Locate every Plasmodium vivax-infected red blood cell.
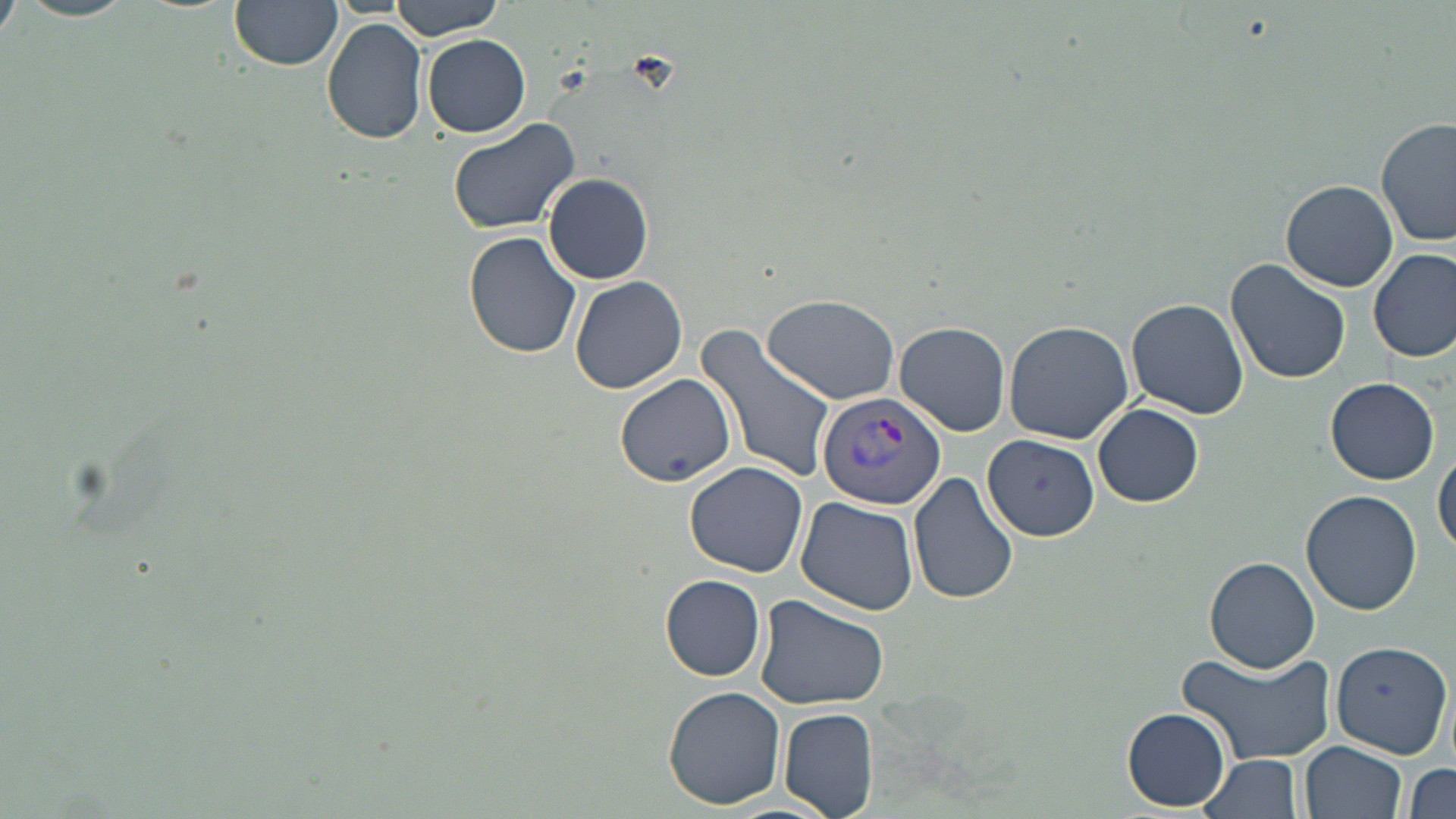

Approximate bounding boxes as named x1/y1/x2/y2 corners in pixels.
Plasmodium vivax-infected red blood cells: (x1=817, y1=392, x2=947, y2=510).

Uninfected red blood cell locations: (x1=385, y1=0, x2=509, y2=39), (x1=0, y1=1, x2=22, y2=43), (x1=229, y1=1, x2=342, y2=70), (x1=322, y1=18, x2=428, y2=144), (x1=422, y1=34, x2=531, y2=138), (x1=446, y1=117, x2=580, y2=234), (x1=1376, y1=117, x2=1456, y2=248), (x1=543, y1=174, x2=654, y2=284), (x1=1282, y1=180, x2=1398, y2=292), (x1=463, y1=231, x2=583, y2=358), (x1=1369, y1=246, x2=1456, y2=364), (x1=1225, y1=259, x2=1351, y2=385), (x1=569, y1=274, x2=688, y2=394), (x1=761, y1=292, x2=900, y2=404), (x1=1126, y1=296, x2=1249, y2=420), (x1=1003, y1=318, x2=1133, y2=444), (x1=696, y1=322, x2=836, y2=484), (x1=896, y1=322, x2=1011, y2=436), (x1=615, y1=372, x2=736, y2=487), (x1=1326, y1=377, x2=1440, y2=486), (x1=1094, y1=402, x2=1204, y2=507), (x1=984, y1=434, x2=1100, y2=542), (x1=1433, y1=449, x2=1455, y2=557), (x1=684, y1=461, x2=807, y2=577), (x1=909, y1=470, x2=1021, y2=607), (x1=1301, y1=490, x2=1422, y2=615), (x1=795, y1=497, x2=918, y2=614), (x1=1206, y1=557, x2=1320, y2=672), (x1=661, y1=575, x2=767, y2=681), (x1=754, y1=594, x2=891, y2=709), (x1=1330, y1=640, x2=1452, y2=757), (x1=1173, y1=646, x2=1336, y2=764), (x1=661, y1=685, x2=786, y2=810), (x1=780, y1=707, x2=879, y2=819), (x1=1123, y1=707, x2=1230, y2=811), (x1=1300, y1=740, x2=1408, y2=819), (x1=1200, y1=754, x2=1304, y2=819), (x1=1406, y1=762, x2=1455, y2=817). Slide-level diagnosis: Plasmodium vivax. Image is 1456×819 pixels. Thin blood smear. May-Grünwald-Giemsa stain. Single field of view. Light microscopy. Captured at 1000x magnification.